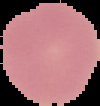
From a thin blood smear. Cell region segmented out of the field of view; the surrounding area is masked to black. Image is 100×106 pixels. Result: negative for malaria parasites.